Classify this cell by malaria status.
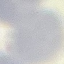

Uninfected.

Summary:
  - Image type: automatically extracted cell patch, resized to 64 × 64 pixels
  - Capture: smartphone camera at the microscope eyepiece
  - Stain: Giemsa
  - Preparation: thin blood smear